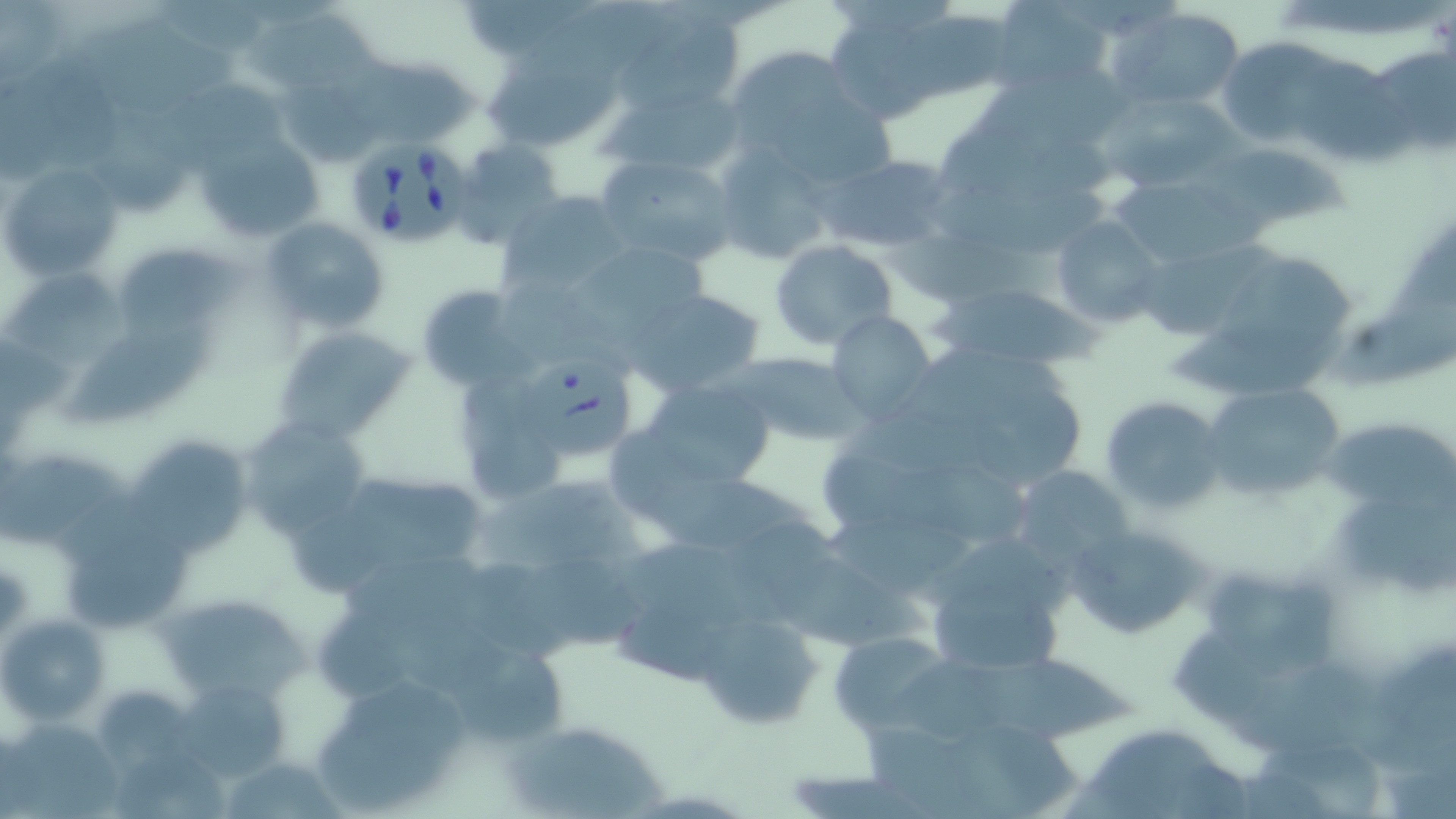
Summary:
  - Coordinate format: approximate bounding boxes as named x1/y1/x2/y2 corners in pixels
  - Uninfected red blood cell locations: (x1=989, y1=0, x2=1113, y2=93), (x1=1, y1=1, x2=68, y2=88), (x1=505, y1=3, x2=674, y2=85), (x1=1117, y1=7, x2=1244, y2=110), (x1=882, y1=15, x2=1021, y2=106), (x1=248, y1=16, x2=395, y2=95), (x1=71, y1=19, x2=244, y2=113), (x1=618, y1=20, x2=744, y2=110), (x1=1219, y1=37, x2=1365, y2=147), (x1=718, y1=47, x2=881, y2=180), (x1=354, y1=54, x2=479, y2=146), (x1=1295, y1=62, x2=1416, y2=164), (x1=491, y1=63, x2=633, y2=153), (x1=977, y1=69, x2=1142, y2=150), (x1=607, y1=82, x2=747, y2=178), (x1=1099, y1=95, x2=1261, y2=193), (x1=95, y1=111, x2=198, y2=215), (x1=193, y1=128, x2=328, y2=246), (x1=712, y1=141, x2=835, y2=265), (x1=455, y1=142, x2=563, y2=243), (x1=1192, y1=142, x2=1357, y2=233), (x1=820, y1=152, x2=958, y2=254), (x1=596, y1=155, x2=739, y2=268), (x1=1, y1=162, x2=122, y2=281), (x1=1108, y1=174, x2=1252, y2=270), (x1=928, y1=180, x2=1110, y2=261), (x1=500, y1=192, x2=626, y2=293), (x1=1052, y1=216, x2=1165, y2=330), (x1=258, y1=217, x2=389, y2=334), (x1=768, y1=239, x2=897, y2=351), (x1=1130, y1=240, x2=1262, y2=345), (x1=123, y1=243, x2=255, y2=335), (x1=569, y1=246, x2=720, y2=329), (x1=1215, y1=255, x2=1362, y2=368), (x1=8, y1=273, x2=138, y2=362), (x1=930, y1=281, x2=1097, y2=375), (x1=415, y1=285, x2=527, y2=394), (x1=628, y1=288, x2=767, y2=396), (x1=1329, y1=305, x2=1455, y2=387), (x1=828, y1=311, x2=936, y2=422), (x1=273, y1=325, x2=414, y2=444), (x1=63, y1=328, x2=217, y2=426), (x1=729, y1=350, x2=865, y2=446), (x1=637, y1=380, x2=778, y2=489), (x1=1197, y1=383, x2=1349, y2=502), (x1=971, y1=385, x2=1087, y2=492), (x1=1100, y1=396, x2=1225, y2=514), (x1=1322, y1=413, x2=1456, y2=521), (x1=240, y1=418, x2=374, y2=537), (x1=465, y1=422, x2=564, y2=506), (x1=124, y1=433, x2=255, y2=553), (x1=821, y1=452, x2=1046, y2=549), (x1=0, y1=457, x2=124, y2=547), (x1=1010, y1=466, x2=1134, y2=570), (x1=333, y1=468, x2=494, y2=582), (x1=638, y1=472, x2=818, y2=553), (x1=483, y1=484, x2=658, y2=572), (x1=1064, y1=522, x2=1212, y2=641), (x1=827, y1=524, x2=979, y2=595), (x1=71, y1=533, x2=192, y2=630), (x1=508, y1=563, x2=653, y2=648), (x1=1205, y1=576, x2=1344, y2=692), (x1=158, y1=588, x2=308, y2=703), (x1=934, y1=588, x2=1066, y2=679), (x1=694, y1=612, x2=824, y2=733), (x1=317, y1=613, x2=429, y2=708), (x1=1, y1=615, x2=109, y2=727), (x1=828, y1=633, x2=956, y2=734), (x1=444, y1=639, x2=571, y2=749), (x1=970, y1=660, x2=1139, y2=741), (x1=311, y1=675, x2=472, y2=815), (x1=171, y1=676, x2=292, y2=785), (x1=97, y1=694, x2=196, y2=776), (x1=3, y1=718, x2=118, y2=815), (x1=504, y1=718, x2=668, y2=819), (x1=861, y1=723, x2=1025, y2=811), (x1=1082, y1=729, x2=1223, y2=819), (x1=1256, y1=745, x2=1385, y2=819), (x1=218, y1=758, x2=348, y2=816)
  - Platelet locations: (x1=286, y1=510, x2=392, y2=597)
  - Babesia divergens-infected red blood cell locations: (x1=344, y1=139, x2=473, y2=250), (x1=517, y1=355, x2=634, y2=459)
  - Slide-level diagnosis: Babesia divergens
  - Preparation: thin blood film
  - Modality: light microscopy
  - Image size: 1456×819 pixels
  - Magnification: 1000x
  - Field of view: single
  - Stain: May-Grünwald-Giemsa